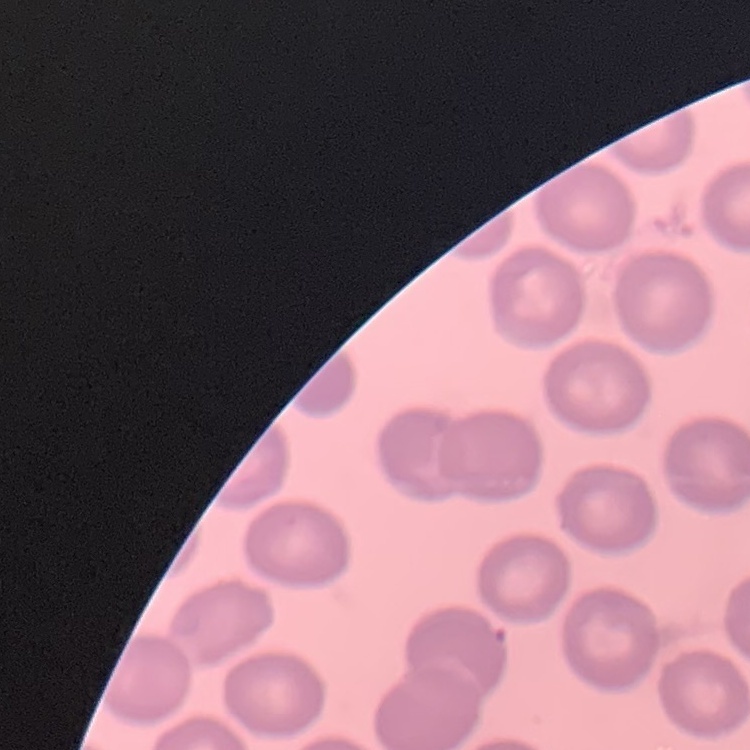

The erythrocytes show no rouleaux formation. Field's or Giemsa stain. Square crop of a larger photomicrograph. Thin blood film.